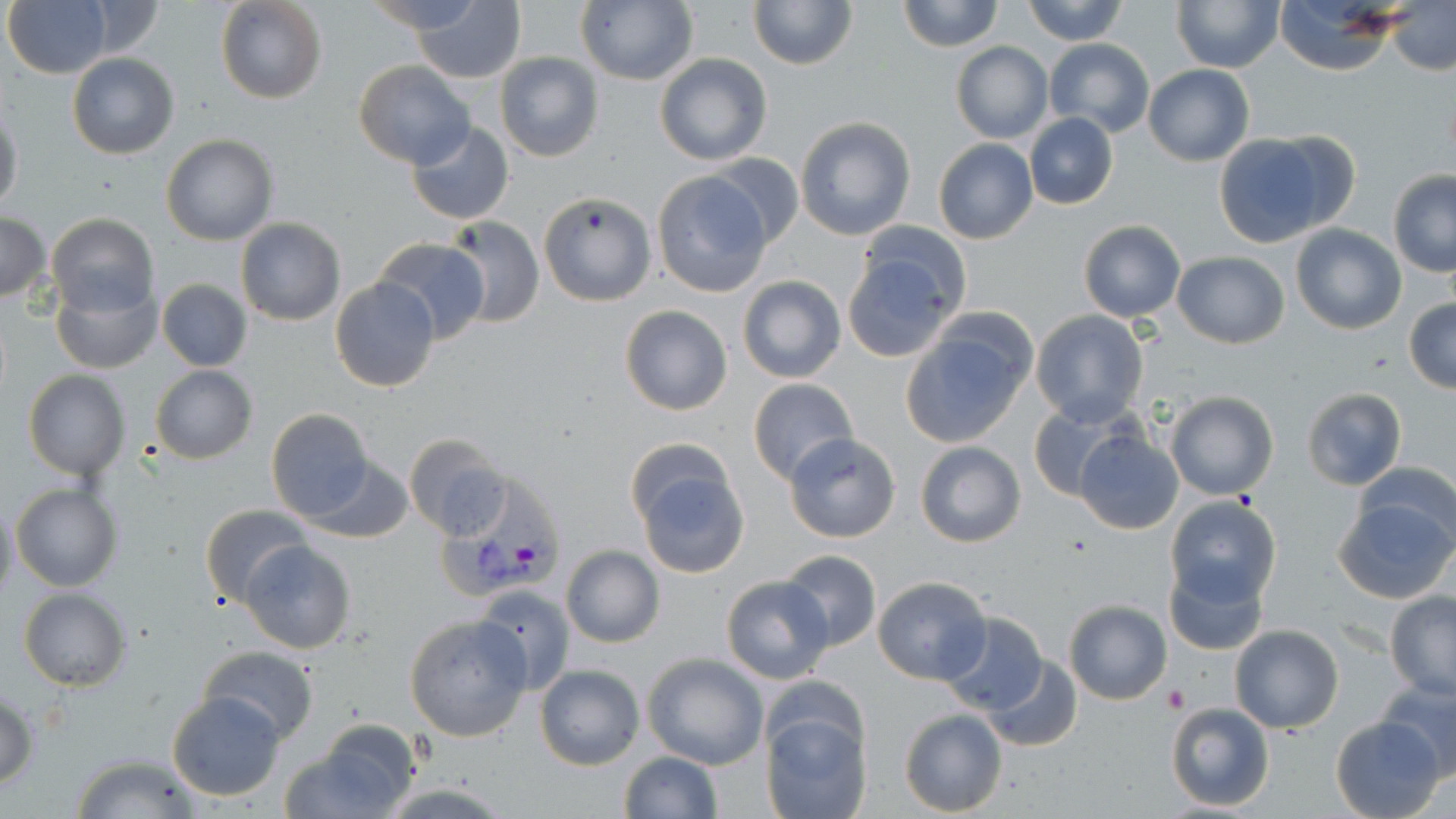

slide-level diagnosis = Plasmodium vivax
field of view = one of a larger specimen
preparation = thin blood smear
platelet locations = approximate bounding boxes as (x1, y1, x2, y2) in pixels: (1163, 682, 1191, 710)
image size = 1456×819 pixels
modality = optical microscopy
Plasmodium vivax-infected red blood cell locations = approximate bounding boxes as (x1, y1, x2, y2) in pixels: (432, 460, 566, 607)
stain = May-Grünwald-Giemsa
uninfected red blood cell locations = approximate bounding boxes as (x1, y1, x2, y2) in pixels: (5, 0, 112, 78), (216, 0, 328, 104), (749, 0, 856, 70), (1020, 0, 1129, 45), (1172, 0, 1283, 72), (897, 1, 1003, 51), (1272, 1, 1404, 76), (411, 2, 525, 83), (575, 2, 699, 86), (1386, 3, 1455, 76), (1044, 37, 1154, 139), (950, 42, 1052, 144), (67, 53, 179, 159), (495, 53, 604, 163), (654, 54, 773, 167), (354, 60, 474, 169), (1143, 64, 1254, 165), (0, 108, 24, 212), (1024, 113, 1118, 211), (795, 116, 918, 241), (406, 120, 514, 225), (1263, 130, 1359, 233), (160, 133, 279, 246), (1214, 134, 1335, 247), (933, 139, 1038, 245), (707, 153, 803, 248), (1388, 169, 1456, 277), (652, 171, 774, 297), (538, 192, 656, 306), (0, 212, 51, 303), (47, 213, 159, 318), (440, 216, 544, 328), (236, 217, 345, 326), (1077, 220, 1186, 323), (1289, 223, 1406, 334), (370, 237, 490, 343), (840, 244, 964, 362), (1172, 251, 1289, 347), (736, 275, 847, 385), (330, 277, 440, 393), (156, 279, 252, 372), (51, 282, 161, 375), (1402, 296, 1456, 393), (620, 304, 733, 415), (1030, 310, 1148, 427), (901, 317, 1035, 448), (150, 364, 257, 463), (23, 370, 130, 480), (747, 379, 858, 486), (1300, 388, 1408, 488), (1164, 390, 1279, 499), (1027, 401, 1136, 503), (265, 409, 375, 523), (1071, 426, 1184, 536), (785, 433, 901, 541), (404, 434, 511, 542), (915, 441, 1026, 548), (627, 447, 753, 579), (305, 455, 413, 543), (1355, 463, 1456, 554), (11, 482, 122, 592), (1164, 495, 1282, 607), (1331, 496, 1456, 607), (0, 500, 18, 603), (199, 503, 311, 609), (242, 540, 357, 654), (561, 545, 664, 648), (779, 549, 881, 651), (1164, 560, 1268, 656), (720, 574, 833, 683), (872, 575, 993, 685), (474, 584, 577, 696), (19, 589, 130, 691), (1385, 591, 1456, 701), (1063, 599, 1172, 705), (936, 611, 1048, 715), (403, 613, 532, 742), (1230, 625, 1344, 732), (198, 645, 320, 743), (643, 654, 768, 770), (984, 656, 1082, 750), (534, 664, 644, 769), (1375, 680, 1456, 777), (166, 691, 285, 802), (1, 694, 39, 790), (1166, 702, 1275, 811), (898, 708, 1007, 816), (761, 712, 870, 819), (1331, 716, 1444, 818), (291, 719, 424, 819), (617, 751, 723, 819), (69, 755, 205, 817)
magnification = 1000x